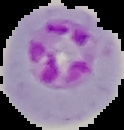
Summary:
  - Result: Plasmodium parasites detected
  - Image size: 124×130 pixels
  - Preparation: thin blood film
  - Image type: segmented cell region on a black background